State the blood parasite species.
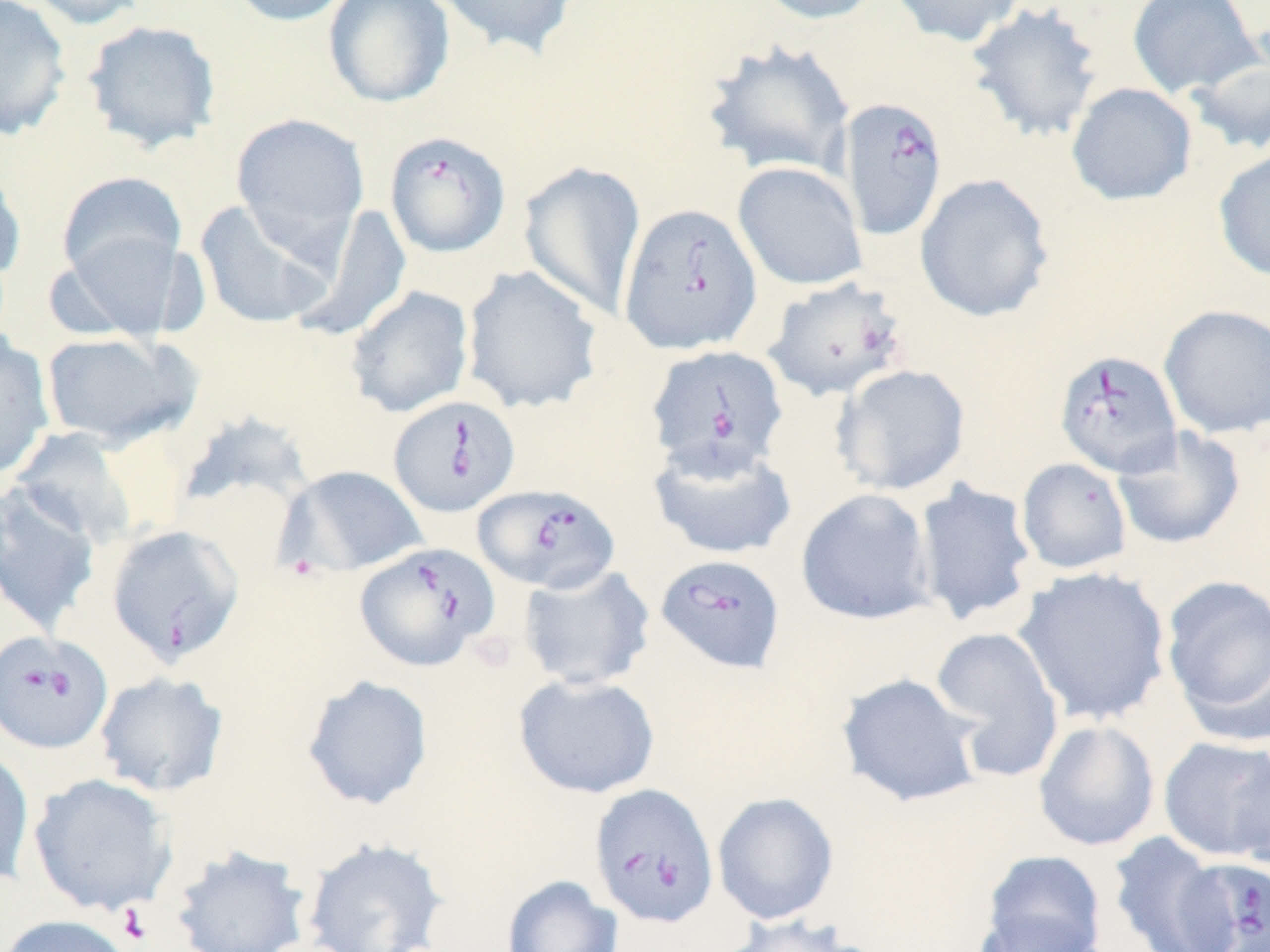

Babesia divergens.

{
  "preparation": "thin blood film",
  "platelet_locations": "approximate bounding boxes as (x1,y1)-(x2,y2) corner pairs in pixels: (116,904)-(156,946)",
  "babesia_divergens_infected_red_blood_cell_locations": "approximate bounding boxes as (x1,y1)-(x2,y2) corner pairs in pixels: (839,96)-(948,240), (384,130)-(512,258), (618,202)-(763,355), (763,276)-(910,403), (645,344)-(789,476), (1054,349)-(1182,478), (388,395)-(520,517), (473,484)-(621,594), (106,524)-(245,668), (354,542)-(500,672), (655,553)-(786,674), (0,630)-(113,755), (590,783)-(719,928), (1175,857)-(1270,952)",
  "magnification": "1000x",
  "uninfected_red_blood_cell_locations": "approximate bounding boxes as (x1,y1)-(x2,y2) corner pairs in pixels: (0,0)-(72,140), (21,0)-(152,30), (224,0)-(358,26), (323,0)-(456,109), (431,0)-(580,61), (753,0)-(886,24), (887,0)-(1026,48), (1127,0)-(1263,100), (965,2)-(1106,143), (82,19)-(222,153), (701,38)-(856,179), (1187,43)-(1269,156), (1066,82)-(1197,206), (231,113)-(370,247), (1213,149)-(1270,282), (0,160)-(26,283), (518,161)-(647,320), (732,161)-(867,291), (56,171)-(187,285), (914,173)-(1055,323), (194,199)-(338,330), (294,204)-(412,342), (56,231)-(189,342), (461,265)-(604,415), (344,285)-(475,419), (1158,304)-(1270,439), (40,331)-(200,449), (0,333)-(55,481), (831,363)-(972,497), (181,419)-(319,506), (1112,427)-(1246,550), (10,428)-(138,547), (648,439)-(798,560), (1016,457)-(1133,574), (283,465)-(429,576), (912,478)-(1038,627), (0,484)-(101,636), (795,487)-(936,626), (517,563)-(657,691), (1013,566)-(1172,726), (1160,574)-(1270,736), (928,625)-(1066,782), (93,670)-(230,798), (835,672)-(987,808), (513,673)-(661,799), (301,674)-(434,811), (1032,719)-(1160,852), (1158,735)-(1270,862), (0,745)-(35,889), (1230,754)-(1270,877), (28,772)-(177,917), (712,791)-(839,925), (1106,831)-(1233,952), (301,836)-(451,952), (169,844)-(314,952), (979,849)-(1107,952), (501,875)-(623,952), (971,910)-(1110,952), (0,914)-(136,952), (715,915)-(867,952)",
  "field_of_view": "single",
  "image_size": "1270×952 pixels",
  "modality": "optical microscopy",
  "stain": "May-Grünwald-Giemsa"
}